Assess the morphology of the erythrocytes.
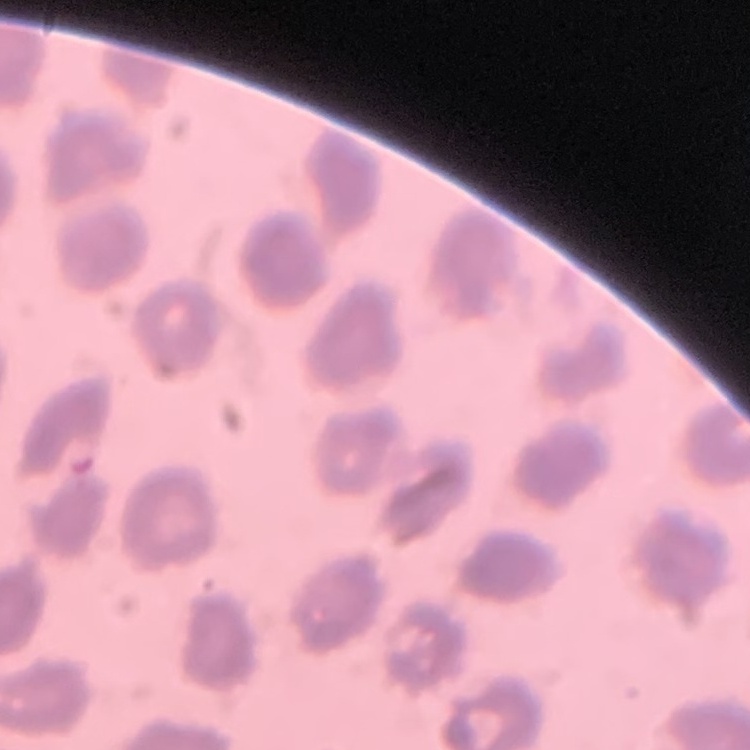

No rouleaux formation.

stain = Field's or Giemsa
image type = one tile cut from a larger photomicrograph
preparation = thin blood smear